State which cell type is depicted.
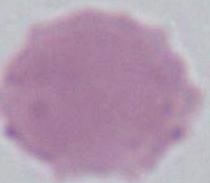

An erythrocyte.

Micrograph. Captured at 1000x magnification.